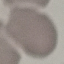
Malaria status: uninfected. Acquired by smartphone through the microscope eyepiece. Automatically extracted cell patch, resized to 64 × 64 pixels. Thin smear of blood. Giemsa-stained preparation.